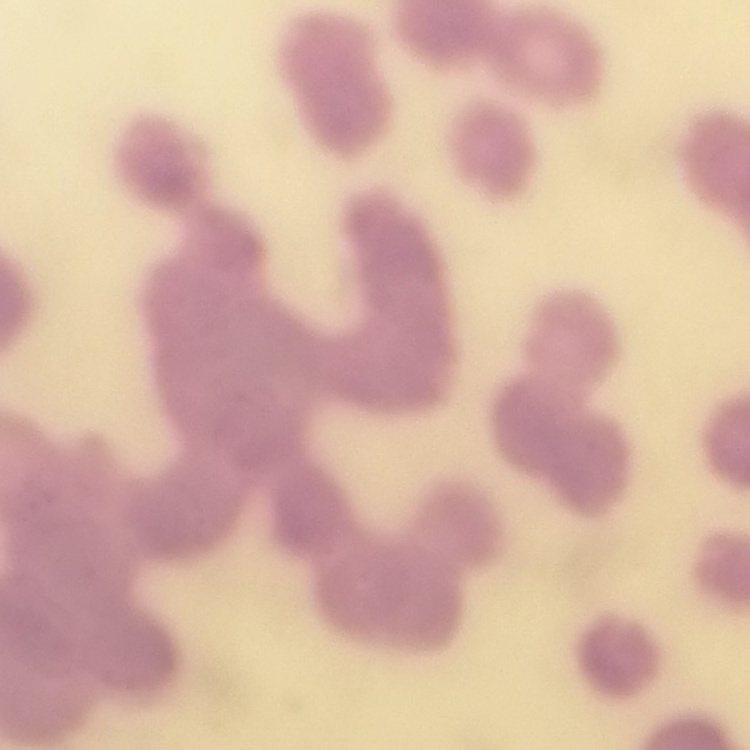
The erythrocytes show rouleaux formation. Thin blood smear. Stained with either Field's or Giemsa. Square crop of a larger photomicrograph.